Give the position of every malaria parasite.
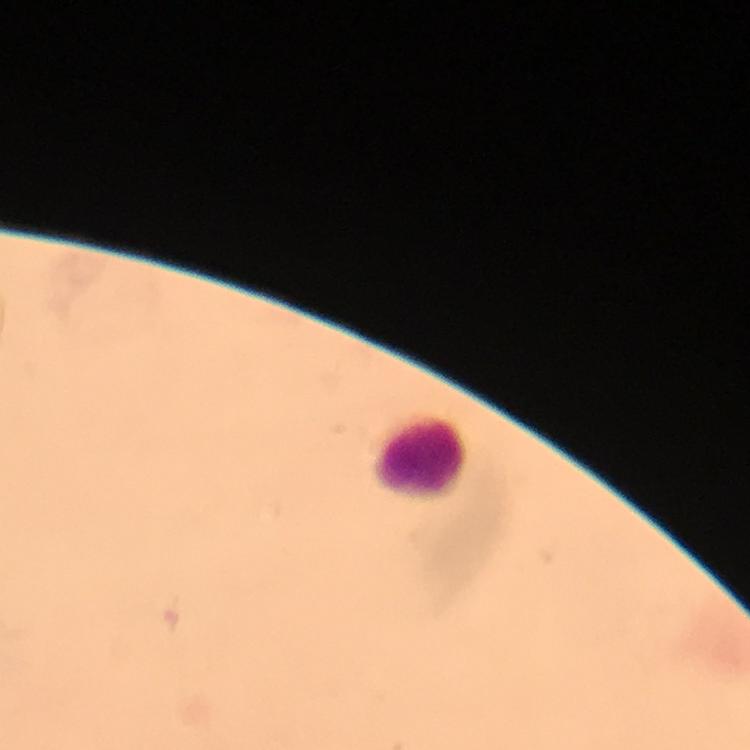
No malaria parasites seen.

Approximate object centers, in pixels from the top-left corner. Leukocyte locations: (x=419, y=450). Thick blood smear. Giemsa-stained preparation. From a malaria diagnostic workup. Image is 750×750 pixels. Immersion oil was used. Cropped region of a single field of view. At 100x magnification. Photographed through the microscope with a smartphone camera.